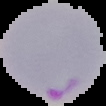

Summary:
  - Image size: 106×106 pixels
  - Image type: cell region segmented out of the field of view; surrounding area masked to black
  - Preparation: thin blood film
  - Malaria status: parasitized